Classify this cell by malaria status.
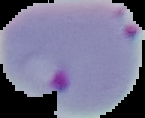

Parasitized.

Image is 145×118 pixels. From a thin blood film. Segmented cell region on a black background.